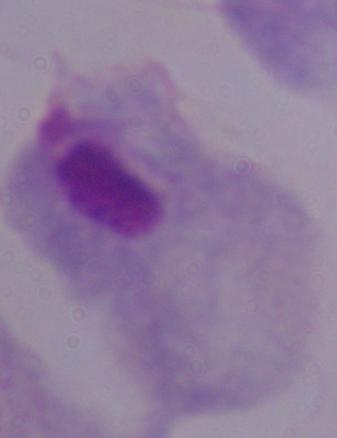

Summary:
  - Magnification: 1000x
  - Identification: trichomonad
  - Modality: photomicrograph